State which cell type is depicted.
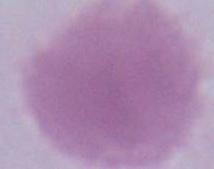
This is an erythrocyte.

Summary:
  - Magnification: 1000x
  - Modality: micrograph